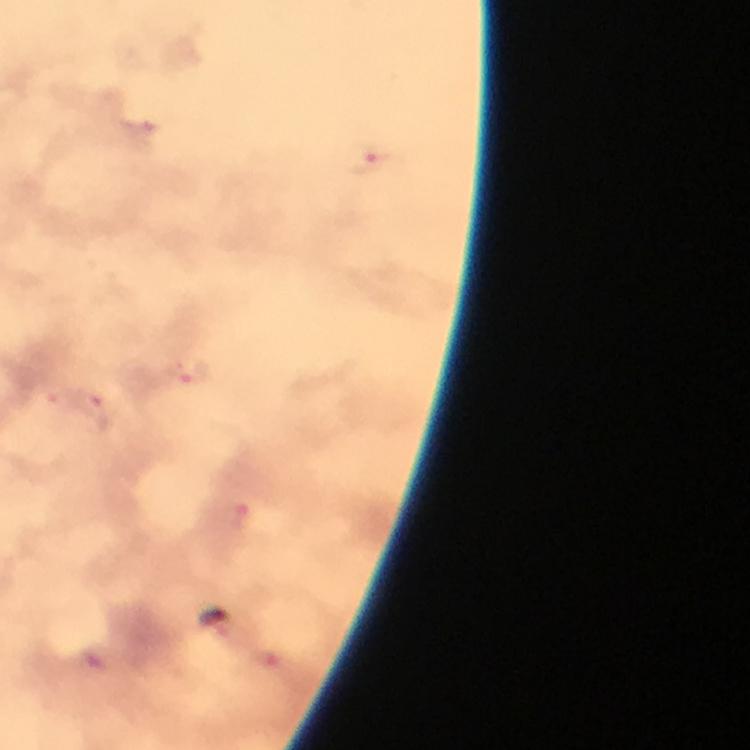 Approximate object centers, in pixels from the top-left corner. Malaria parasite locations: (x=372, y=158), (x=186, y=370), (x=90, y=407), (x=242, y=516). Cropped region of a single field of view. Image is 750×750 pixels. Thick blood film. 100x magnification. Immersion oil applied. From a malaria diagnostic workup. Photographed with a smartphone mounted on the microscope. Giemsa stain.